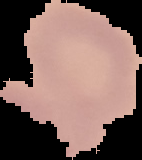

image type = cell region segmented out of the field of view; surrounding area masked to black
result = no malaria parasites detected
image size = 142×160 pixels
preparation = thin blood film